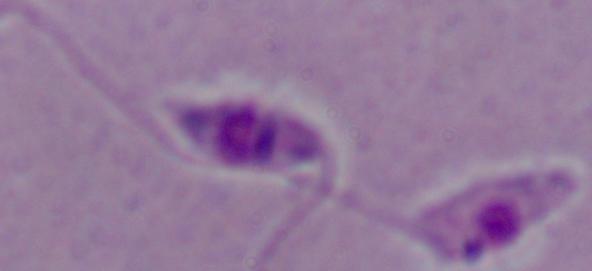 Captured at 1000x magnification. A Leishmania parasite is seen. Micrograph.